Describe the morphology of the erythrocytes.
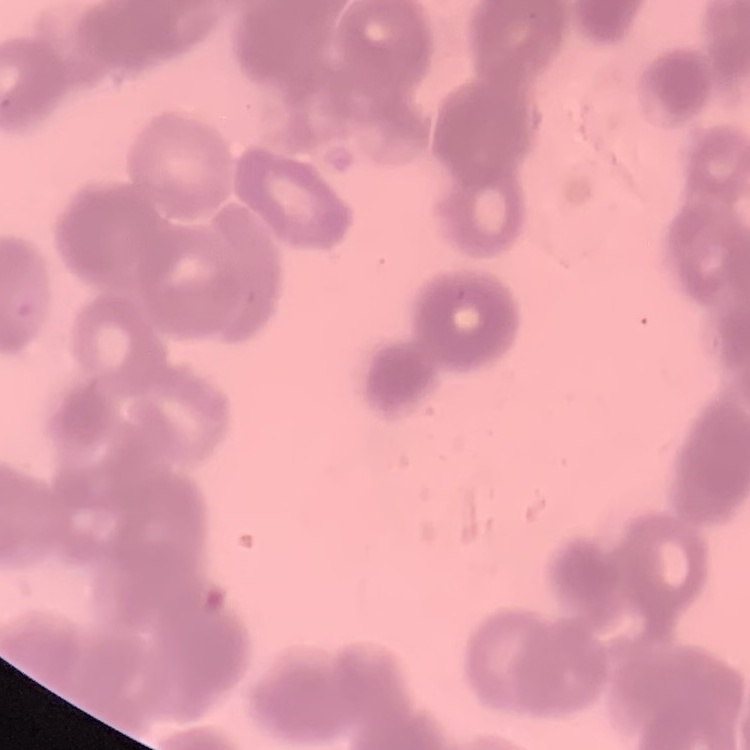

They show rouleaux formation.

Summary:
  - Stain: Field's or Giemsa
  - Image type: square crop of a larger photomicrograph
  - Preparation: thin peripheral smear